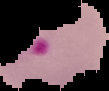
From a thin blood film. Malaria status: parasitized. The area outside the segmented cell region is set to black. Image is 109×91 pixels.